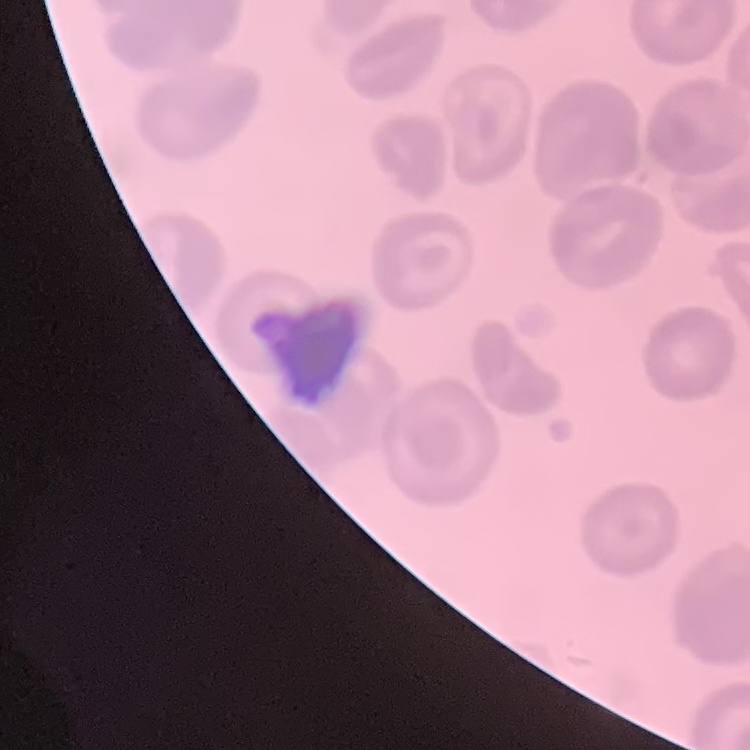
The erythrocytes exhibit no rouleaux formation. One tile cut from a larger photomicrograph. Thin blood smear. Stained with either Field's or Giemsa.